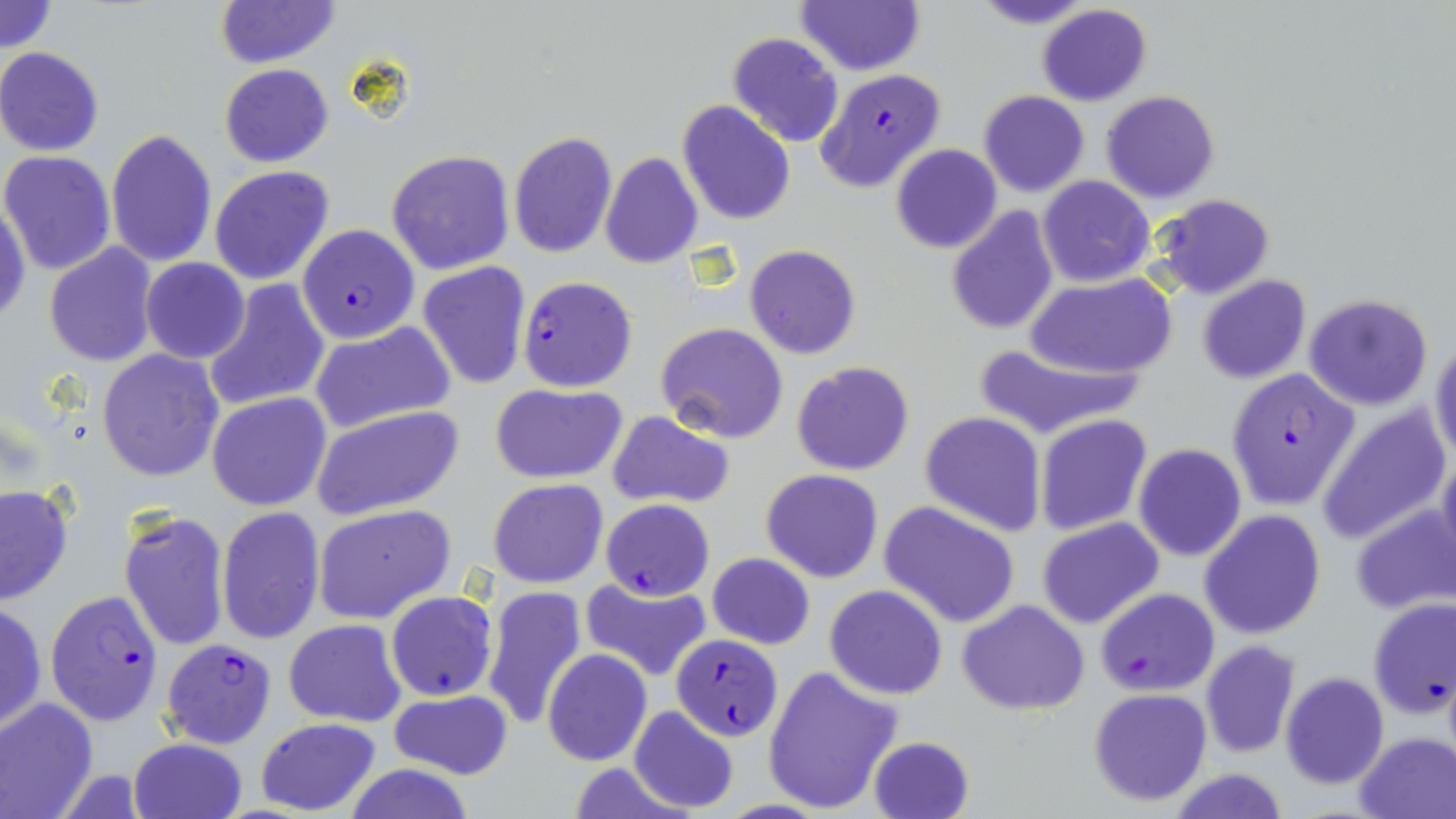
Summary:
  - Coordinate format: approximate bounding boxes as named x1/y1/x2/y2 corners in pixels
  - Plasmodium falciparum-infected red blood cell locations: (x1=815, y1=68, x2=946, y2=193), (x1=296, y1=224, x2=419, y2=344), (x1=518, y1=275, x2=637, y2=392), (x1=1224, y1=367, x2=1361, y2=511), (x1=601, y1=498, x2=715, y2=601), (x1=1094, y1=587, x2=1219, y2=695), (x1=45, y1=589, x2=165, y2=724), (x1=672, y1=632, x2=783, y2=741), (x1=159, y1=637, x2=278, y2=749)
  - Uninfected red blood cell locations: (x1=0, y1=0, x2=56, y2=54), (x1=969, y1=0, x2=1096, y2=30), (x1=215, y1=1, x2=338, y2=69), (x1=796, y1=1, x2=925, y2=76), (x1=1035, y1=4, x2=1153, y2=108), (x1=727, y1=32, x2=845, y2=148), (x1=0, y1=46, x2=105, y2=157), (x1=219, y1=64, x2=333, y2=167), (x1=979, y1=90, x2=1089, y2=198), (x1=1101, y1=90, x2=1219, y2=204), (x1=677, y1=100, x2=796, y2=225), (x1=105, y1=129, x2=217, y2=269), (x1=508, y1=130, x2=617, y2=258), (x1=891, y1=143, x2=1002, y2=254), (x1=386, y1=149, x2=514, y2=275), (x1=0, y1=151, x2=116, y2=275), (x1=600, y1=152, x2=702, y2=269), (x1=209, y1=166, x2=334, y2=285), (x1=1038, y1=176, x2=1155, y2=287), (x1=1149, y1=194, x2=1275, y2=299), (x1=1, y1=199, x2=31, y2=327), (x1=946, y1=206, x2=1061, y2=335), (x1=44, y1=242, x2=160, y2=369), (x1=744, y1=243, x2=861, y2=358), (x1=141, y1=256, x2=250, y2=364), (x1=417, y1=261, x2=531, y2=391), (x1=1028, y1=274, x2=1174, y2=380), (x1=1196, y1=274, x2=1310, y2=385), (x1=202, y1=278, x2=330, y2=413), (x1=1302, y1=292, x2=1434, y2=411), (x1=308, y1=322, x2=456, y2=434), (x1=655, y1=323, x2=788, y2=444), (x1=1430, y1=338, x2=1456, y2=466), (x1=969, y1=342, x2=1145, y2=441), (x1=96, y1=347, x2=225, y2=482), (x1=792, y1=360, x2=913, y2=475), (x1=490, y1=383, x2=627, y2=484), (x1=207, y1=392, x2=332, y2=510), (x1=1316, y1=403, x2=1452, y2=543), (x1=310, y1=404, x2=465, y2=520), (x1=607, y1=410, x2=735, y2=511), (x1=919, y1=411, x2=1046, y2=537), (x1=1036, y1=413, x2=1152, y2=536), (x1=1134, y1=443, x2=1247, y2=563), (x1=1436, y1=446, x2=1456, y2=571), (x1=761, y1=469, x2=883, y2=583), (x1=488, y1=477, x2=609, y2=588), (x1=0, y1=483, x2=73, y2=605), (x1=879, y1=501, x2=1023, y2=628), (x1=1349, y1=503, x2=1456, y2=614), (x1=312, y1=505, x2=457, y2=624), (x1=216, y1=507, x2=326, y2=644), (x1=118, y1=508, x2=231, y2=652), (x1=1200, y1=510, x2=1326, y2=641), (x1=1037, y1=517, x2=1164, y2=630), (x1=706, y1=554, x2=816, y2=650), (x1=579, y1=577, x2=712, y2=681), (x1=482, y1=585, x2=587, y2=730), (x1=824, y1=585, x2=947, y2=699), (x1=385, y1=591, x2=497, y2=703), (x1=1367, y1=597, x2=1456, y2=720), (x1=958, y1=600, x2=1090, y2=715), (x1=1, y1=602, x2=47, y2=733), (x1=284, y1=619, x2=407, y2=727), (x1=1200, y1=641, x2=1299, y2=757), (x1=542, y1=649, x2=652, y2=765), (x1=762, y1=664, x2=902, y2=815), (x1=1281, y1=671, x2=1389, y2=788), (x1=1088, y1=687, x2=1214, y2=806), (x1=388, y1=689, x2=514, y2=780), (x1=0, y1=697, x2=99, y2=817), (x1=628, y1=705, x2=739, y2=814), (x1=254, y1=717, x2=381, y2=815), (x1=1355, y1=731, x2=1456, y2=817), (x1=868, y1=734, x2=976, y2=819), (x1=128, y1=737, x2=249, y2=819), (x1=343, y1=762, x2=478, y2=819), (x1=1167, y1=768, x2=1289, y2=819)
  - Slide-level diagnosis: Plasmodium falciparum
  - Stain: May-Grünwald-Giemsa
  - Modality: optical microscopy
  - Field of view: one of a larger specimen
  - Magnification: 1000x
  - Preparation: thin blood film
  - Image size: 1456×819 pixels